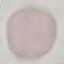

malaria status = uninfected
stain = Giemsa
capture = smartphone through the microscope eyepiece
preparation = thin blood smear
image type = automatically extracted cell patch, resized to 64 × 64 pixels